Outline platelets.
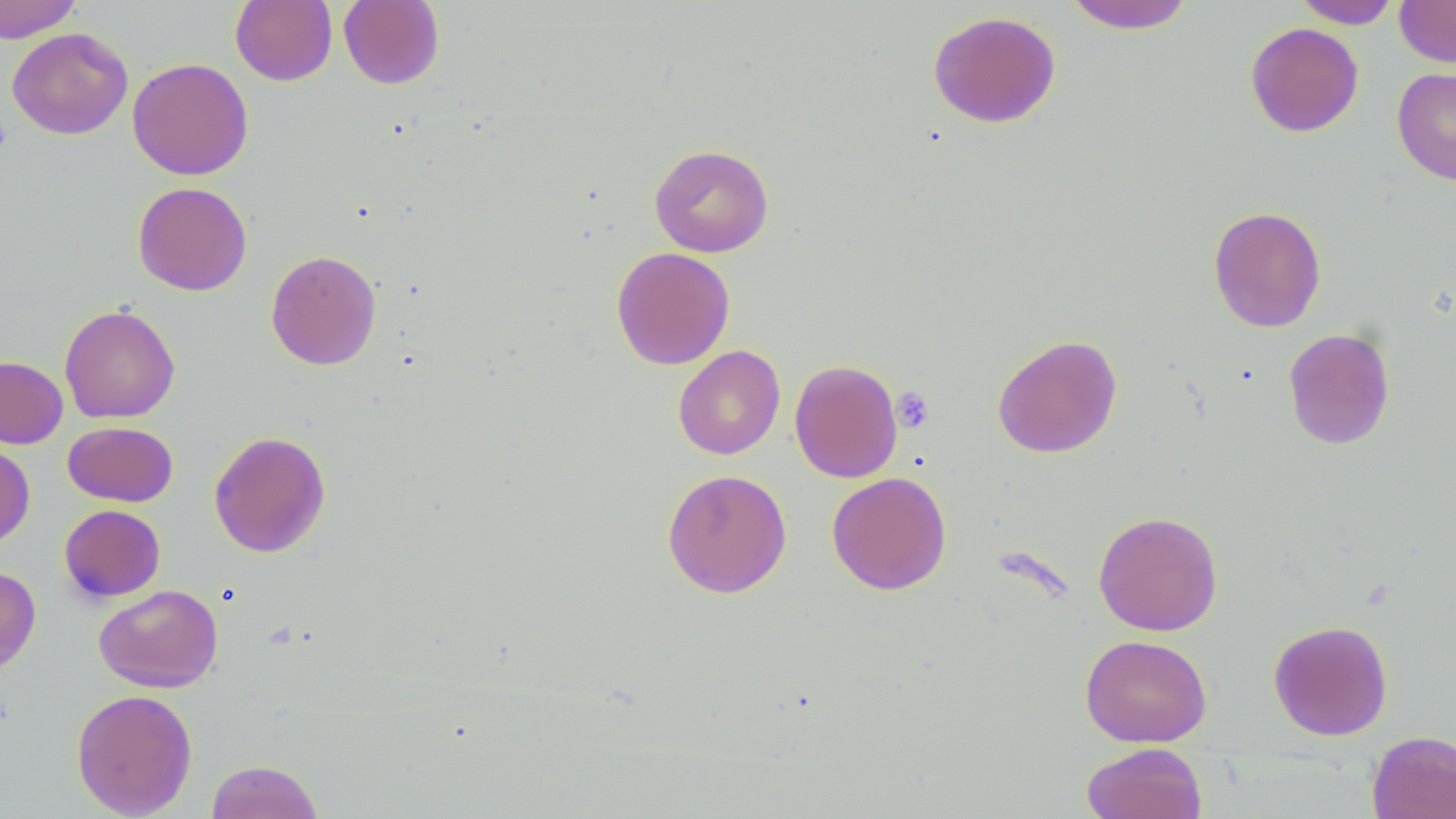
Approximate bounding boxes as (x1, y1, x2, y2) in pixels.
Platelets: (0, 115, 11, 158), (892, 387, 934, 432).

Summary:
  - Uninfected red blood cell locations: (0, 0, 83, 43), (230, 0, 337, 86), (1062, 0, 1197, 34), (1291, 0, 1402, 28), (1395, 0, 1456, 67), (338, 1, 445, 89), (928, 10, 1062, 128), (1245, 22, 1364, 137), (7, 27, 133, 140), (127, 57, 253, 180), (1392, 66, 1456, 185), (649, 143, 774, 257), (132, 182, 252, 296), (1207, 205, 1326, 332), (611, 247, 735, 370), (265, 249, 382, 370), (59, 303, 180, 423), (1283, 327, 1396, 450), (992, 334, 1122, 458), (673, 345, 785, 460), (0, 356, 68, 448), (789, 359, 903, 482), (62, 421, 178, 506), (208, 430, 331, 558), (0, 440, 35, 548), (662, 468, 792, 598), (826, 471, 951, 595), (59, 504, 166, 602), (1093, 510, 1223, 636), (0, 565, 41, 674), (93, 584, 224, 692), (1268, 620, 1394, 741), (1080, 634, 1212, 748), (71, 688, 198, 817), (1367, 730, 1456, 819), (1081, 743, 1208, 819), (205, 759, 324, 819)
  - Slide-level diagnosis: no evidence of blood parasites
  - Modality: light microscopy
  - Image size: 1456×819 pixels
  - Field of view: one of a larger specimen
  - Preparation: thin blood film
  - Magnification: 1000x
  - Stain: May-Grünwald-Giemsa